Report the malaria status of this cell.
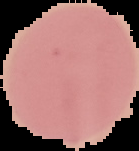
It is uninfected.

image_type: cell region segmented out of the field of view; surrounding area masked to black
preparation: thin blood smear
image_size: 139×151 pixels